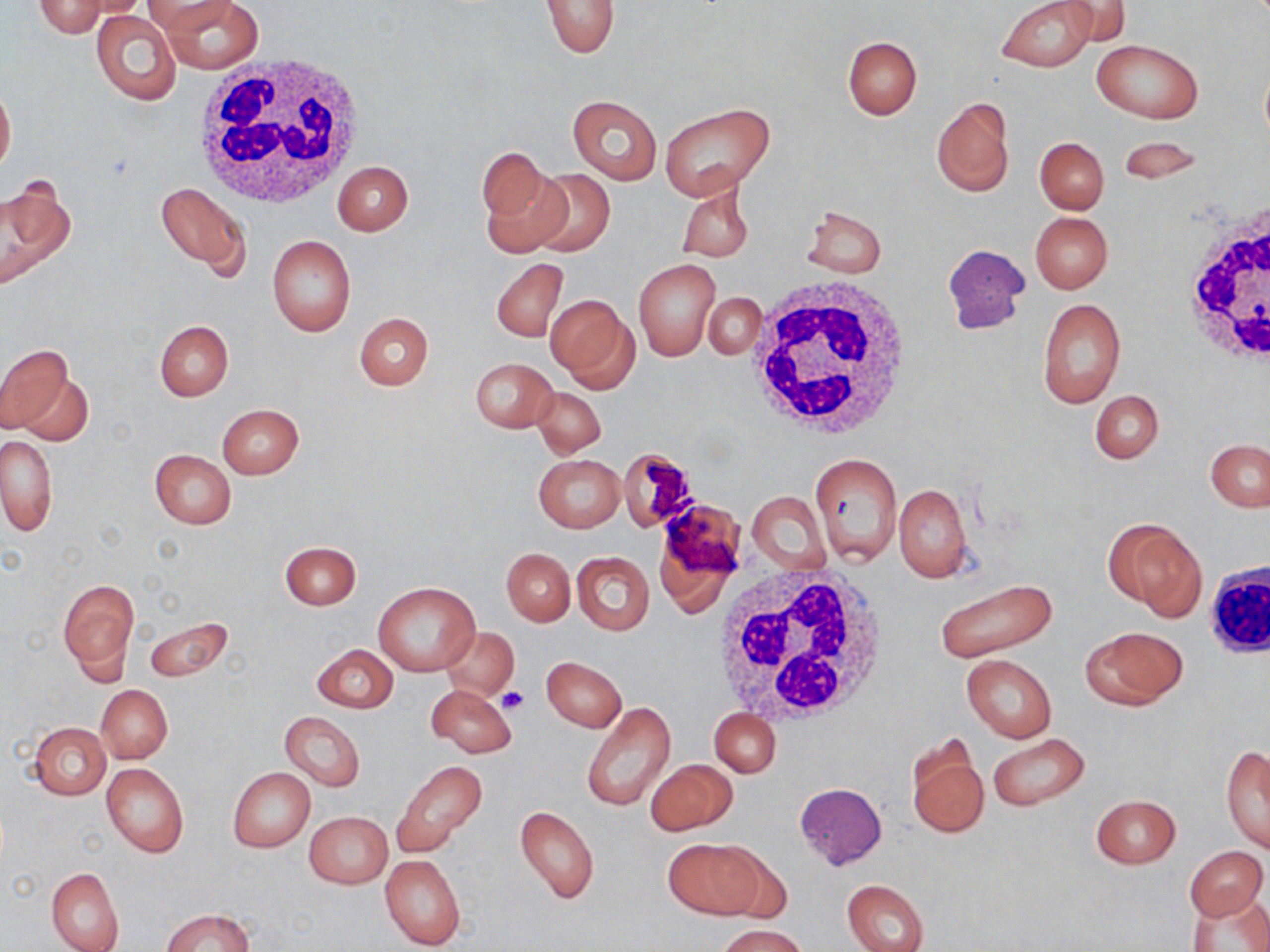
Summary:
  - Coordinate format: approximate bounding boxes as named x1/y1/x2/y2 corners in pixels
  - White blood cell locations: (x1=196, y1=53, x2=369, y2=208), (x1=1175, y1=196, x2=1270, y2=372), (x1=747, y1=275, x2=912, y2=443), (x1=1204, y1=558, x2=1270, y2=663), (x1=712, y1=562, x2=889, y2=730)
  - Platelet locations: (x1=498, y1=686, x2=529, y2=716)
  - Uninfected red blood cell locations: (x1=32, y1=0, x2=110, y2=37), (x1=141, y1=0, x2=232, y2=34), (x1=163, y1=0, x2=262, y2=73), (x1=995, y1=0, x2=1097, y2=72), (x1=1049, y1=0, x2=1131, y2=48), (x1=540, y1=1, x2=619, y2=58), (x1=91, y1=9, x2=180, y2=105), (x1=843, y1=36, x2=922, y2=120), (x1=1091, y1=40, x2=1203, y2=124), (x1=0, y1=81, x2=15, y2=176), (x1=567, y1=93, x2=662, y2=185), (x1=930, y1=96, x2=1015, y2=197), (x1=661, y1=103, x2=775, y2=201), (x1=1117, y1=135, x2=1204, y2=185), (x1=1035, y1=137, x2=1108, y2=214), (x1=477, y1=146, x2=550, y2=229), (x1=332, y1=161, x2=414, y2=235), (x1=479, y1=167, x2=573, y2=259), (x1=528, y1=168, x2=615, y2=257), (x1=0, y1=176, x2=75, y2=290), (x1=155, y1=180, x2=251, y2=275), (x1=678, y1=183, x2=753, y2=261), (x1=802, y1=207, x2=886, y2=277), (x1=1030, y1=212, x2=1113, y2=293), (x1=266, y1=235, x2=355, y2=336), (x1=942, y1=243, x2=1030, y2=335), (x1=492, y1=258, x2=568, y2=343), (x1=633, y1=259, x2=720, y2=361), (x1=546, y1=294, x2=637, y2=391), (x1=704, y1=294, x2=766, y2=359), (x1=1036, y1=297, x2=1125, y2=408), (x1=354, y1=312, x2=433, y2=390), (x1=154, y1=319, x2=233, y2=401), (x1=0, y1=345, x2=80, y2=441), (x1=469, y1=357, x2=557, y2=433), (x1=532, y1=387, x2=606, y2=457), (x1=1090, y1=390, x2=1164, y2=464), (x1=218, y1=404, x2=303, y2=479), (x1=0, y1=436, x2=58, y2=536), (x1=1206, y1=440, x2=1270, y2=511), (x1=149, y1=448, x2=235, y2=529), (x1=812, y1=451, x2=903, y2=565), (x1=533, y1=454, x2=625, y2=533), (x1=894, y1=482, x2=971, y2=582), (x1=747, y1=491, x2=829, y2=575), (x1=1108, y1=519, x2=1204, y2=618), (x1=280, y1=541, x2=362, y2=610), (x1=502, y1=548, x2=575, y2=626), (x1=572, y1=551, x2=654, y2=635), (x1=934, y1=577, x2=1055, y2=662), (x1=59, y1=579, x2=138, y2=682), (x1=374, y1=583, x2=478, y2=677), (x1=144, y1=615, x2=232, y2=683), (x1=1081, y1=626, x2=1187, y2=708), (x1=440, y1=627, x2=519, y2=700), (x1=312, y1=644, x2=398, y2=713), (x1=962, y1=654, x2=1057, y2=742), (x1=542, y1=656, x2=627, y2=731), (x1=96, y1=684, x2=172, y2=763), (x1=426, y1=684, x2=519, y2=758), (x1=581, y1=700, x2=676, y2=812), (x1=710, y1=708, x2=780, y2=778), (x1=280, y1=711, x2=364, y2=790), (x1=29, y1=723, x2=110, y2=799), (x1=986, y1=732, x2=1090, y2=811), (x1=905, y1=735, x2=988, y2=842), (x1=1221, y1=744, x2=1270, y2=852), (x1=646, y1=759, x2=738, y2=835), (x1=393, y1=761, x2=487, y2=860), (x1=102, y1=763, x2=188, y2=857), (x1=228, y1=767, x2=315, y2=852), (x1=794, y1=782, x2=887, y2=869), (x1=1090, y1=793, x2=1182, y2=869), (x1=514, y1=805, x2=600, y2=904), (x1=303, y1=811, x2=392, y2=890), (x1=664, y1=838, x2=768, y2=919), (x1=1183, y1=845, x2=1267, y2=920), (x1=380, y1=854, x2=464, y2=950), (x1=46, y1=866, x2=124, y2=952), (x1=842, y1=878, x2=930, y2=952), (x1=1187, y1=893, x2=1270, y2=952), (x1=161, y1=908, x2=254, y2=952), (x1=717, y1=925, x2=808, y2=952)
  - Slide-level diagnosis: negative for blood parasites
  - Image size: 1270×952 pixels
  - Stain: May-Grünwald-Giemsa
  - Preparation: thin blood film
  - Modality: light microscopy
  - Field of view: one of a larger specimen
  - Magnification: 1000x